Outline platelets.
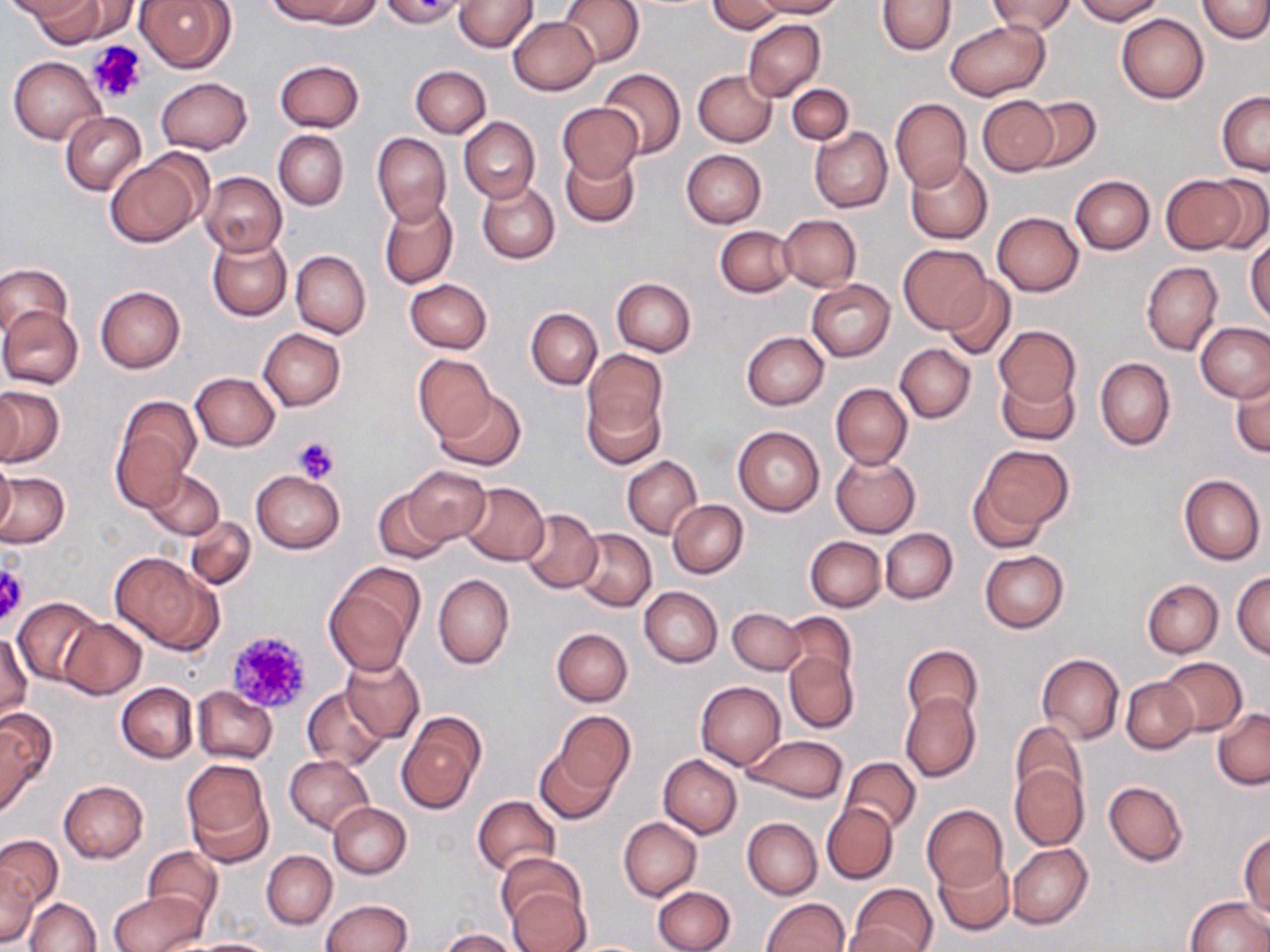
Approximate bounding boxes as named x1/y1/x2/y2 corners in pixels.
Platelets: (x1=87, y1=40, x2=148, y2=104), (x1=293, y1=434, x2=340, y2=484), (x1=0, y1=563, x2=28, y2=630), (x1=224, y1=629, x2=315, y2=715).

Summary:
  - Uninfected red blood cell locations: (x1=17, y1=0, x2=107, y2=43), (x1=54, y1=0, x2=141, y2=42), (x1=135, y1=0, x2=236, y2=73), (x1=378, y1=0, x2=466, y2=26), (x1=454, y1=0, x2=538, y2=51), (x1=558, y1=0, x2=643, y2=66), (x1=707, y1=0, x2=784, y2=34), (x1=755, y1=0, x2=842, y2=17), (x1=877, y1=0, x2=954, y2=55), (x1=987, y1=0, x2=1075, y2=36), (x1=1073, y1=0, x2=1164, y2=24), (x1=1199, y1=0, x2=1270, y2=43), (x1=274, y1=1, x2=375, y2=27), (x1=1117, y1=14, x2=1208, y2=103), (x1=507, y1=17, x2=599, y2=95), (x1=742, y1=19, x2=824, y2=102), (x1=946, y1=20, x2=1047, y2=101), (x1=8, y1=55, x2=105, y2=146), (x1=275, y1=59, x2=364, y2=131), (x1=410, y1=65, x2=491, y2=137), (x1=598, y1=68, x2=685, y2=159), (x1=693, y1=69, x2=776, y2=147), (x1=155, y1=77, x2=252, y2=154), (x1=787, y1=84, x2=853, y2=145), (x1=1217, y1=91, x2=1269, y2=175), (x1=977, y1=95, x2=1059, y2=176), (x1=1021, y1=97, x2=1101, y2=172), (x1=890, y1=98, x2=971, y2=191), (x1=557, y1=102, x2=643, y2=183), (x1=59, y1=111, x2=147, y2=196), (x1=458, y1=117, x2=539, y2=204), (x1=810, y1=127, x2=892, y2=212), (x1=274, y1=130, x2=349, y2=210), (x1=371, y1=131, x2=451, y2=226), (x1=560, y1=149, x2=640, y2=228), (x1=681, y1=149, x2=767, y2=227), (x1=106, y1=150, x2=207, y2=247), (x1=905, y1=157, x2=992, y2=244), (x1=199, y1=171, x2=287, y2=257), (x1=1163, y1=175, x2=1252, y2=254), (x1=1203, y1=175, x2=1270, y2=252), (x1=1071, y1=176, x2=1154, y2=254), (x1=476, y1=181, x2=560, y2=263), (x1=378, y1=198, x2=458, y2=289), (x1=991, y1=211, x2=1083, y2=296), (x1=778, y1=214, x2=861, y2=290), (x1=715, y1=225, x2=795, y2=297), (x1=207, y1=235, x2=291, y2=322), (x1=1246, y1=236, x2=1270, y2=324), (x1=898, y1=244, x2=992, y2=333), (x1=289, y1=250, x2=370, y2=339), (x1=1140, y1=262, x2=1222, y2=355), (x1=0, y1=263, x2=71, y2=339), (x1=943, y1=276, x2=1015, y2=359), (x1=612, y1=277, x2=697, y2=356), (x1=405, y1=278, x2=492, y2=353), (x1=806, y1=279, x2=896, y2=361), (x1=95, y1=286, x2=185, y2=373), (x1=0, y1=306, x2=83, y2=389), (x1=526, y1=307, x2=602, y2=390), (x1=1196, y1=322, x2=1270, y2=401), (x1=994, y1=326, x2=1080, y2=404), (x1=258, y1=329, x2=346, y2=410), (x1=740, y1=331, x2=828, y2=409), (x1=895, y1=343, x2=975, y2=422), (x1=581, y1=350, x2=668, y2=452), (x1=412, y1=354, x2=496, y2=441), (x1=1095, y1=357, x2=1176, y2=451), (x1=1230, y1=371, x2=1269, y2=458), (x1=190, y1=372, x2=280, y2=450), (x1=996, y1=372, x2=1078, y2=444), (x1=830, y1=383, x2=912, y2=468), (x1=0, y1=385, x2=63, y2=467), (x1=434, y1=388, x2=526, y2=472), (x1=0, y1=390, x2=22, y2=465), (x1=111, y1=394, x2=200, y2=506), (x1=733, y1=426, x2=825, y2=516), (x1=973, y1=444, x2=1073, y2=535), (x1=830, y1=454, x2=920, y2=537), (x1=1, y1=456, x2=15, y2=538), (x1=622, y1=457, x2=702, y2=539), (x1=403, y1=466, x2=490, y2=545), (x1=145, y1=469, x2=225, y2=539), (x1=251, y1=470, x2=345, y2=553), (x1=0, y1=473, x2=69, y2=548), (x1=1178, y1=474, x2=1265, y2=566), (x1=967, y1=475, x2=1051, y2=554), (x1=461, y1=482, x2=549, y2=565), (x1=373, y1=489, x2=452, y2=565), (x1=668, y1=500, x2=747, y2=577), (x1=520, y1=508, x2=602, y2=594), (x1=185, y1=515, x2=256, y2=591), (x1=880, y1=528, x2=957, y2=604), (x1=573, y1=529, x2=656, y2=610), (x1=805, y1=536, x2=885, y2=612), (x1=979, y1=550, x2=1068, y2=633), (x1=109, y1=553, x2=221, y2=653), (x1=324, y1=563, x2=424, y2=673), (x1=1232, y1=571, x2=1270, y2=659), (x1=433, y1=574, x2=513, y2=670), (x1=1142, y1=578, x2=1223, y2=658), (x1=638, y1=587, x2=722, y2=668), (x1=12, y1=596, x2=102, y2=685), (x1=728, y1=607, x2=804, y2=674), (x1=780, y1=613, x2=858, y2=686), (x1=58, y1=619, x2=147, y2=699), (x1=552, y1=628, x2=632, y2=705), (x1=1, y1=634, x2=31, y2=722), (x1=901, y1=644, x2=981, y2=724), (x1=784, y1=653, x2=858, y2=734), (x1=1037, y1=653, x2=1123, y2=745), (x1=341, y1=657, x2=424, y2=742), (x1=1158, y1=657, x2=1246, y2=736), (x1=1121, y1=676, x2=1199, y2=754), (x1=695, y1=682, x2=785, y2=769), (x1=116, y1=683, x2=197, y2=763), (x1=192, y1=686, x2=277, y2=764), (x1=303, y1=686, x2=390, y2=771), (x1=900, y1=692, x2=980, y2=782), (x1=0, y1=708, x2=55, y2=812), (x1=553, y1=710, x2=634, y2=797), (x1=1213, y1=710, x2=1270, y2=789), (x1=397, y1=714, x2=485, y2=816), (x1=1010, y1=720, x2=1088, y2=803), (x1=744, y1=734, x2=847, y2=802), (x1=535, y1=747, x2=618, y2=825), (x1=659, y1=754, x2=741, y2=839), (x1=284, y1=755, x2=373, y2=833), (x1=840, y1=756, x2=921, y2=835), (x1=181, y1=759, x2=274, y2=867), (x1=1009, y1=764, x2=1089, y2=850), (x1=59, y1=780, x2=148, y2=863), (x1=1104, y1=781, x2=1188, y2=866), (x1=472, y1=796, x2=561, y2=878), (x1=328, y1=802, x2=411, y2=879), (x1=822, y1=802, x2=897, y2=883), (x1=922, y1=805, x2=1007, y2=890), (x1=619, y1=817, x2=702, y2=901), (x1=742, y1=818, x2=821, y2=900), (x1=754, y1=831, x2=830, y2=943), (x1=1240, y1=831, x2=1269, y2=917), (x1=0, y1=834, x2=62, y2=909), (x1=1008, y1=843, x2=1092, y2=929), (x1=143, y1=847, x2=223, y2=926), (x1=262, y1=850, x2=336, y2=928), (x1=498, y1=854, x2=587, y2=933), (x1=932, y1=855, x2=1013, y2=936), (x1=0, y1=864, x2=41, y2=948), (x1=850, y1=883, x2=937, y2=952), (x1=505, y1=884, x2=591, y2=952), (x1=653, y1=885, x2=736, y2=952), (x1=109, y1=892, x2=205, y2=952), (x1=1186, y1=896, x2=1269, y2=951), (x1=761, y1=897, x2=848, y2=951), (x1=25, y1=898, x2=101, y2=952), (x1=319, y1=899, x2=412, y2=952), (x1=842, y1=924, x2=927, y2=952), (x1=440, y1=929, x2=520, y2=952), (x1=186, y1=938, x2=278, y2=951)
  - Slide-level diagnosis: negative for blood parasites
  - Field of view: one of a larger specimen
  - Image size: 1270×952 pixels
  - Magnification: 1000x
  - Stain: May-Grünwald-Giemsa
  - Modality: light microscopy
  - Preparation: thin blood film